State which cell type is depicted.
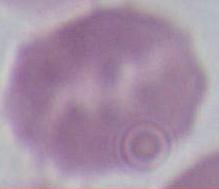
This is an erythrocyte.

Micrograph. 1000x magnification.